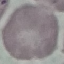

Summary:
  - Malaria status: uninfected
  - Stain: Giemsa
  - Image type: automatically extracted cell patch, resized to 64 × 64 pixels
  - Preparation: thin blood smear
  - Capture: smartphone through the microscope eyepiece